Classify this cell by malaria status.
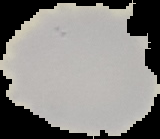
Uninfected.

Summary:
  - Preparation: thin blood smear
  - Image size: 160×139 pixels
  - Image type: segmented cell region on a black background